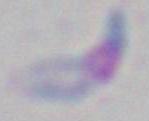

modality = photomicrograph
identification = Toxoplasma gondii
magnification = 1000x